Assess this cell for malaria.
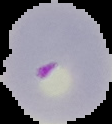

It is parasitized.

Image is 112×124 pixels. The area outside the segmented cell region is set to black. From a thin blood film.